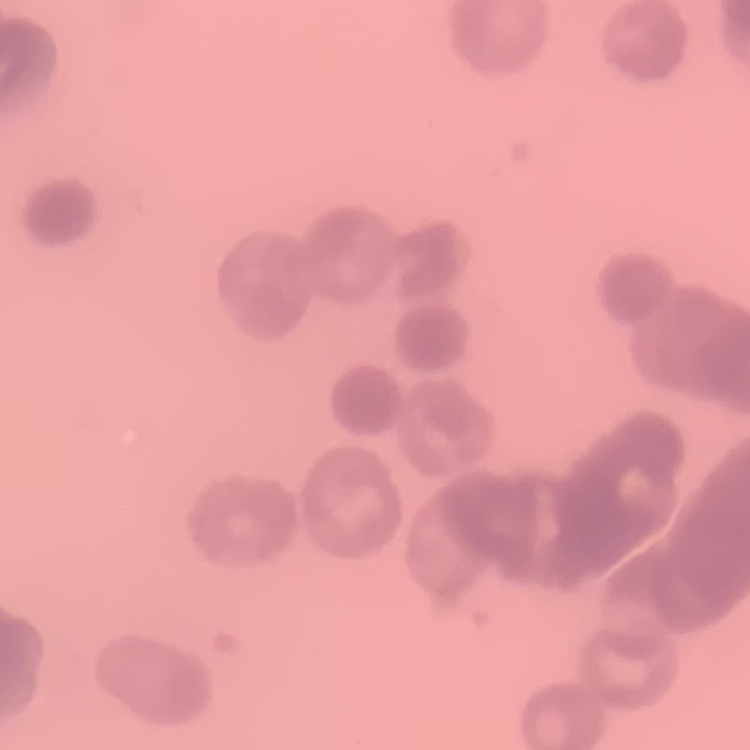
The red blood cells show rouleaux formation. Square crop of a larger photomicrograph. Thin blood smear. Field's or Giemsa stain.